Classify this cell by malaria status.
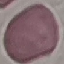
It is uninfected.

stain: Giemsa
capture: smartphone camera at the microscope eyepiece
preparation: thin smear
image_type: cell patch, automatically extracted from a larger field of view and resized to 64 × 64 pixels